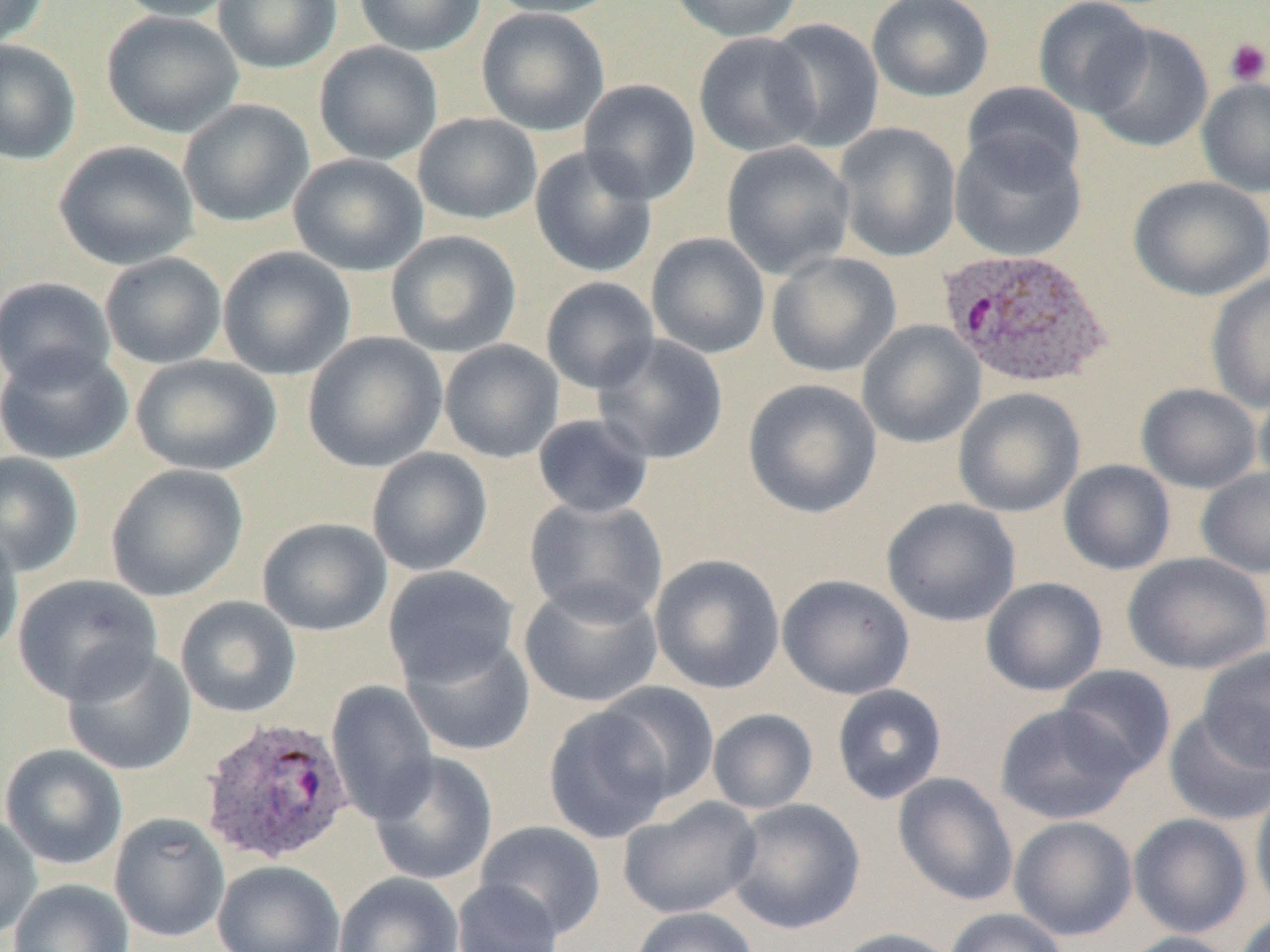

Summary:
  - Coordinate format: approximate bounding boxes as named x1/y1/x2/y2 corners in pixels
  - Uninfected red blood cell locations: (x1=0, y1=0, x2=51, y2=50), (x1=112, y1=0, x2=243, y2=22), (x1=213, y1=0, x2=342, y2=74), (x1=354, y1=0, x2=486, y2=56), (x1=484, y1=0, x2=623, y2=19), (x1=668, y1=0, x2=803, y2=42), (x1=866, y1=0, x2=995, y2=103), (x1=1033, y1=0, x2=1154, y2=117), (x1=476, y1=7, x2=610, y2=136), (x1=101, y1=11, x2=245, y2=138), (x1=764, y1=17, x2=885, y2=152), (x1=1087, y1=23, x2=1213, y2=155), (x1=693, y1=32, x2=823, y2=158), (x1=0, y1=40, x2=81, y2=165), (x1=314, y1=41, x2=444, y2=165), (x1=1196, y1=77, x2=1270, y2=198), (x1=579, y1=78, x2=701, y2=205), (x1=962, y1=82, x2=1086, y2=185), (x1=178, y1=99, x2=314, y2=228), (x1=413, y1=113, x2=543, y2=225), (x1=834, y1=121, x2=962, y2=262), (x1=950, y1=131, x2=1087, y2=262), (x1=53, y1=140, x2=199, y2=270), (x1=721, y1=141, x2=856, y2=279), (x1=528, y1=145, x2=658, y2=278), (x1=288, y1=153, x2=428, y2=276), (x1=1128, y1=175, x2=1270, y2=302), (x1=386, y1=230, x2=522, y2=358), (x1=646, y1=232, x2=771, y2=359), (x1=218, y1=246, x2=356, y2=381), (x1=766, y1=252, x2=902, y2=378), (x1=100, y1=253, x2=228, y2=369), (x1=1206, y1=272, x2=1270, y2=413), (x1=540, y1=276, x2=660, y2=394), (x1=0, y1=277, x2=116, y2=390), (x1=857, y1=320, x2=986, y2=449), (x1=302, y1=331, x2=448, y2=473), (x1=593, y1=334, x2=729, y2=465), (x1=439, y1=339, x2=564, y2=463), (x1=0, y1=344, x2=133, y2=465), (x1=131, y1=354, x2=282, y2=476), (x1=742, y1=378, x2=883, y2=519), (x1=1136, y1=383, x2=1263, y2=493), (x1=1254, y1=383, x2=1270, y2=491), (x1=953, y1=387, x2=1085, y2=518), (x1=532, y1=413, x2=654, y2=520), (x1=366, y1=447, x2=494, y2=576), (x1=0, y1=452, x2=84, y2=577), (x1=1058, y1=459, x2=1176, y2=575), (x1=105, y1=464, x2=249, y2=602), (x1=1196, y1=466, x2=1270, y2=578), (x1=524, y1=496, x2=669, y2=625), (x1=881, y1=498, x2=1021, y2=627), (x1=257, y1=517, x2=392, y2=636), (x1=0, y1=527, x2=24, y2=664), (x1=1123, y1=552, x2=1269, y2=674), (x1=649, y1=554, x2=785, y2=694), (x1=382, y1=565, x2=520, y2=688), (x1=12, y1=574, x2=163, y2=705), (x1=777, y1=574, x2=915, y2=700), (x1=980, y1=577, x2=1108, y2=697), (x1=519, y1=580, x2=663, y2=709), (x1=175, y1=595, x2=301, y2=719), (x1=400, y1=632, x2=536, y2=756), (x1=62, y1=647, x2=196, y2=776), (x1=1197, y1=647, x2=1270, y2=772), (x1=1055, y1=664, x2=1176, y2=780), (x1=326, y1=681, x2=439, y2=824), (x1=592, y1=681, x2=720, y2=806), (x1=831, y1=684, x2=947, y2=804), (x1=994, y1=703, x2=1138, y2=825), (x1=542, y1=704, x2=678, y2=844), (x1=1164, y1=707, x2=1270, y2=826), (x1=707, y1=708, x2=818, y2=814), (x1=1, y1=744, x2=129, y2=870), (x1=369, y1=752, x2=498, y2=886), (x1=892, y1=772, x2=1018, y2=906), (x1=1250, y1=781, x2=1270, y2=919), (x1=618, y1=797, x2=762, y2=919), (x1=725, y1=798, x2=865, y2=935), (x1=0, y1=813, x2=43, y2=940), (x1=109, y1=813, x2=230, y2=942), (x1=1128, y1=813, x2=1253, y2=938), (x1=1010, y1=815, x2=1138, y2=941), (x1=474, y1=821, x2=606, y2=939), (x1=212, y1=860, x2=345, y2=952), (x1=333, y1=872, x2=464, y2=952), (x1=8, y1=879, x2=134, y2=952), (x1=452, y1=879, x2=563, y2=952), (x1=629, y1=906, x2=758, y2=952), (x1=943, y1=908, x2=1070, y2=952), (x1=1234, y1=911, x2=1270, y2=952), (x1=828, y1=927, x2=963, y2=952), (x1=1114, y1=931, x2=1244, y2=952)
  - Platelet locations: (x1=1225, y1=38, x2=1270, y2=86)
  - Plasmodium ovale-infected red blood cell locations: (x1=938, y1=246, x2=1113, y2=390), (x1=198, y1=716, x2=355, y2=866)
  - Slide-level diagnosis: Plasmodium ovale
  - Image size: 1270×952 pixels
  - Modality: optical microscopy
  - Preparation: thin blood smear
  - Magnification: 1000x
  - Field of view: one of a larger specimen